Report the malaria status of this cell.
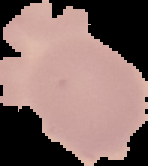

It is uninfected.

Summary:
  - Image size: 148×166 pixels
  - Image type: segmented cell region with the area outside set to black
  - Preparation: thin blood smear